Locate every blood parasite and identify its species.
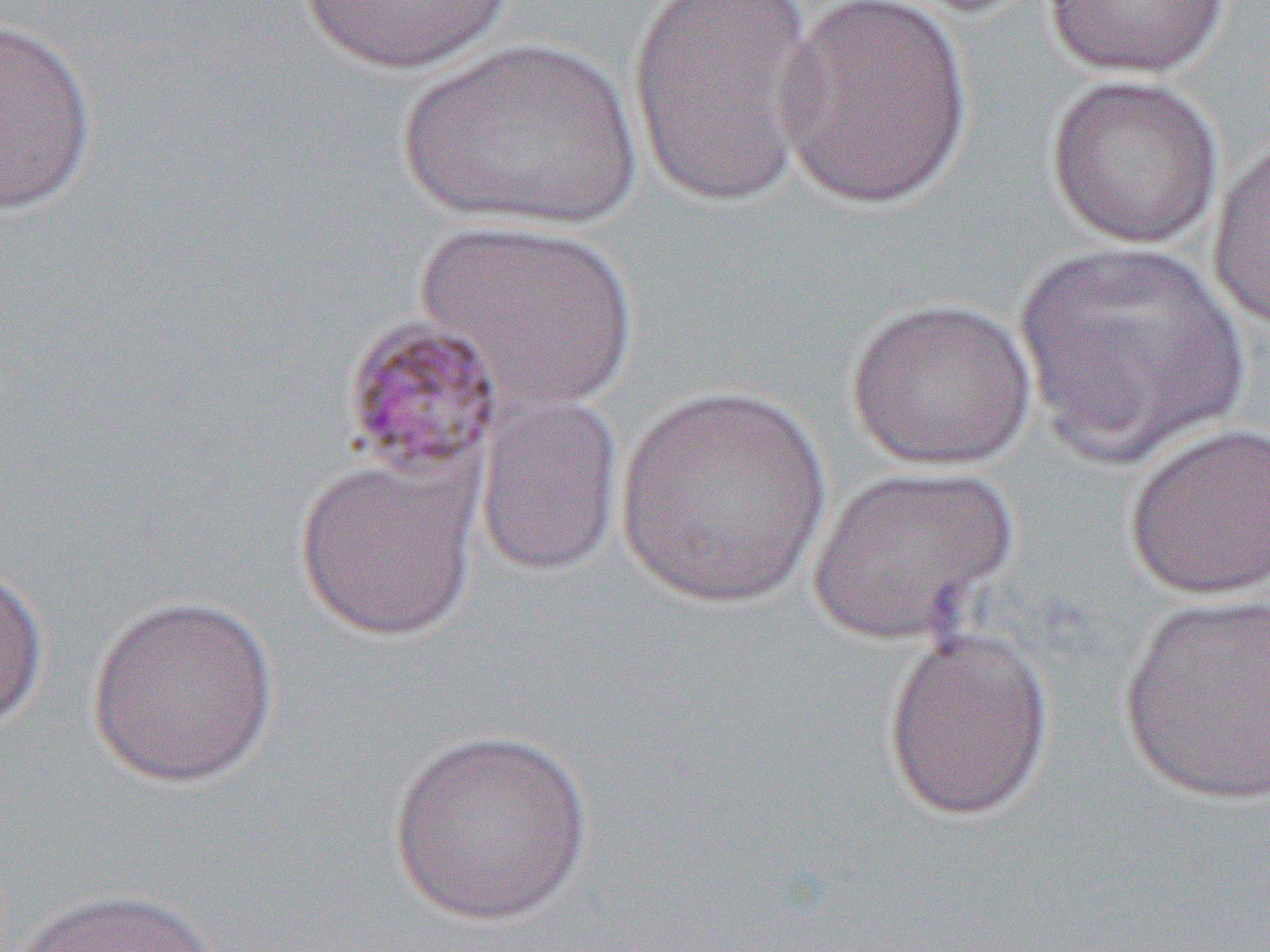
Approximate bounding boxes as (x1,y1)-(x2,y2) corner pairs in pixels.
Plasmodium malariae-infected red blood cells: (340,315)-(506,487).
No Plasmodium falciparum, Plasmodium ovale, Plasmodium vivax, Babesia divergens, or Trypanosoma brucei observed.

Summary:
  - Uninfected red blood cell locations: (772,0)-(974,210), (1041,0)-(1234,78), (296,1)-(516,74), (626,2)-(823,207), (0,18)-(99,216), (393,37)-(644,231), (1044,72)-(1225,249), (1205,133)-(1270,333), (415,219)-(640,412), (1013,241)-(1249,464), (845,296)-(1038,470), (614,382)-(833,610), (473,392)-(625,578), (1122,421)-(1270,601), (293,454)-(483,642), (805,464)-(1019,644), (0,563)-(49,735), (1116,590)-(1270,808), (86,592)-(281,790), (880,625)-(1055,822), (388,726)-(593,925), (12,887)-(222,952)
  - Slide-level diagnosis: Plasmodium malariae
  - Image size: 1270×952 pixels
  - Modality: optical microscopy
  - Preparation: thin blood film
  - Magnification: 1000x
  - Field of view: single